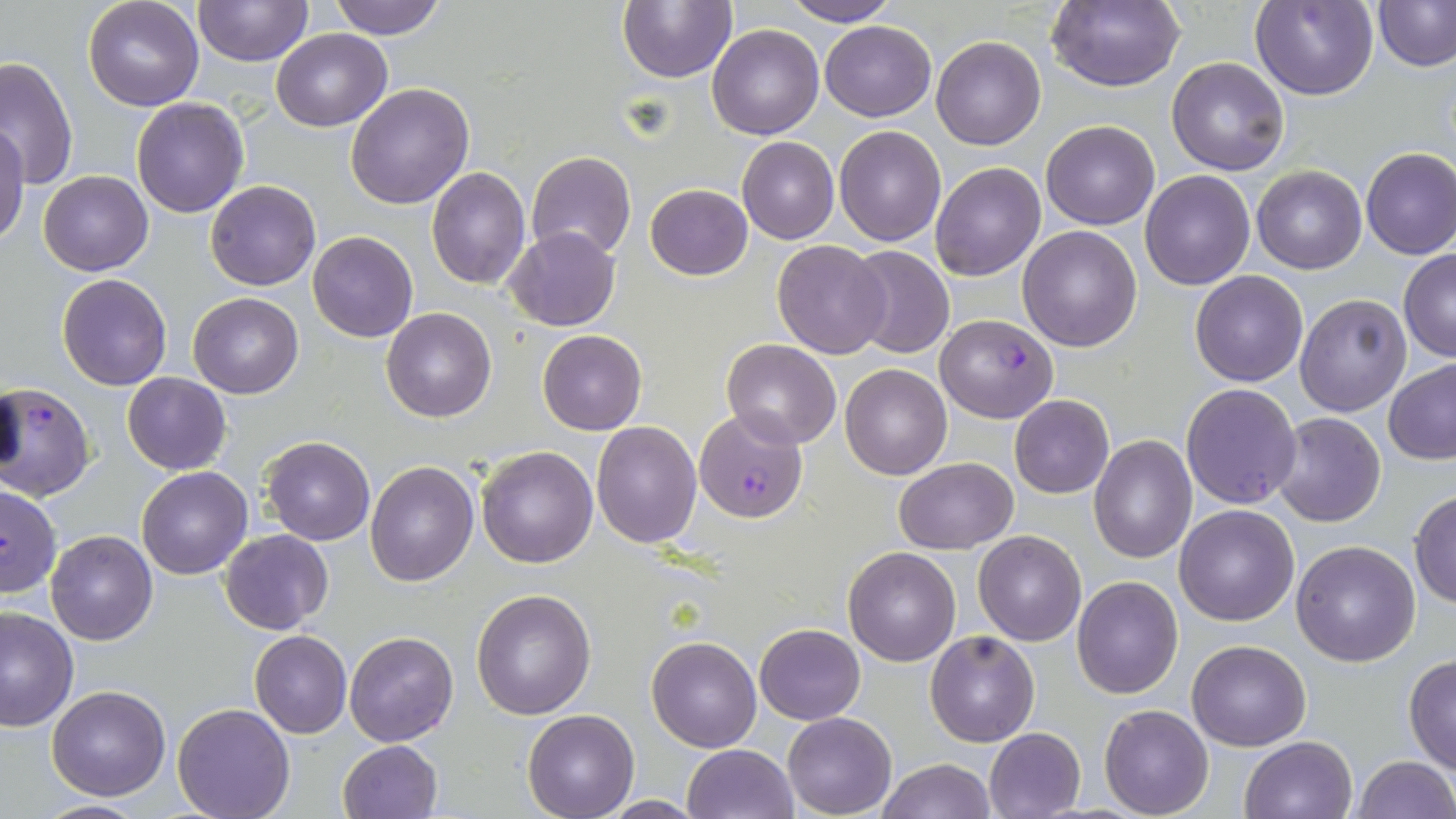
Approximate bounding boxes as named x1/y1/x2/y2 corners in pixels. Plasmodium falciparum-infected red blood cell locations: (x1=935, y1=313, x2=1059, y2=422), (x1=1, y1=382, x2=96, y2=502), (x1=696, y1=407, x2=808, y2=521), (x1=1, y1=483, x2=63, y2=598). Uninfected red blood cell locations: (x1=193, y1=0, x2=311, y2=66), (x1=328, y1=0, x2=448, y2=40), (x1=618, y1=0, x2=737, y2=83), (x1=782, y1=0, x2=900, y2=26), (x1=1253, y1=0, x2=1379, y2=101), (x1=1374, y1=0, x2=1456, y2=71), (x1=82, y1=1, x2=204, y2=111), (x1=1046, y1=1, x2=1186, y2=92), (x1=820, y1=21, x2=936, y2=121), (x1=707, y1=23, x2=824, y2=139), (x1=273, y1=28, x2=391, y2=130), (x1=931, y1=36, x2=1045, y2=151), (x1=0, y1=55, x2=77, y2=191), (x1=1167, y1=56, x2=1289, y2=175), (x1=345, y1=83, x2=474, y2=210), (x1=131, y1=98, x2=249, y2=219), (x1=0, y1=119, x2=30, y2=244), (x1=1041, y1=120, x2=1160, y2=230), (x1=834, y1=127, x2=945, y2=246), (x1=738, y1=137, x2=839, y2=244), (x1=1360, y1=146, x2=1456, y2=260), (x1=526, y1=150, x2=637, y2=261), (x1=930, y1=162, x2=1046, y2=282), (x1=426, y1=167, x2=530, y2=289), (x1=1252, y1=167, x2=1366, y2=274), (x1=1139, y1=169, x2=1256, y2=291), (x1=39, y1=170, x2=153, y2=276), (x1=205, y1=179, x2=321, y2=291), (x1=645, y1=183, x2=752, y2=280), (x1=1017, y1=226, x2=1143, y2=350), (x1=505, y1=227, x2=621, y2=332), (x1=308, y1=230, x2=418, y2=342), (x1=772, y1=239, x2=892, y2=358), (x1=845, y1=245, x2=956, y2=359), (x1=1398, y1=250, x2=1456, y2=360), (x1=1190, y1=270, x2=1307, y2=387), (x1=57, y1=273, x2=172, y2=390), (x1=188, y1=291, x2=303, y2=399), (x1=1294, y1=293, x2=1413, y2=416), (x1=382, y1=308, x2=497, y2=422), (x1=536, y1=329, x2=647, y2=434), (x1=722, y1=338, x2=841, y2=448), (x1=1383, y1=360, x2=1455, y2=464), (x1=841, y1=364, x2=952, y2=480), (x1=121, y1=372, x2=232, y2=475), (x1=1180, y1=383, x2=1302, y2=509), (x1=1009, y1=395, x2=1113, y2=499), (x1=1271, y1=412, x2=1386, y2=527), (x1=591, y1=421, x2=703, y2=549), (x1=261, y1=434, x2=376, y2=545), (x1=1088, y1=436, x2=1197, y2=563), (x1=476, y1=446, x2=599, y2=566), (x1=895, y1=458, x2=1018, y2=553), (x1=366, y1=460, x2=479, y2=586), (x1=137, y1=466, x2=252, y2=580), (x1=1409, y1=489, x2=1456, y2=608), (x1=1173, y1=504, x2=1299, y2=625), (x1=45, y1=529, x2=158, y2=646), (x1=219, y1=529, x2=334, y2=636), (x1=973, y1=530, x2=1086, y2=646), (x1=1290, y1=541, x2=1421, y2=666), (x1=844, y1=546, x2=961, y2=665), (x1=1072, y1=575, x2=1182, y2=699), (x1=472, y1=589, x2=598, y2=720), (x1=0, y1=605, x2=77, y2=731), (x1=754, y1=623, x2=865, y2=724), (x1=925, y1=629, x2=1040, y2=746), (x1=249, y1=630, x2=351, y2=738), (x1=345, y1=630, x2=458, y2=746), (x1=647, y1=637, x2=761, y2=752), (x1=1187, y1=638, x2=1310, y2=750), (x1=1403, y1=655, x2=1456, y2=774), (x1=46, y1=684, x2=172, y2=800), (x1=172, y1=703, x2=294, y2=819), (x1=1100, y1=704, x2=1214, y2=817), (x1=522, y1=710, x2=637, y2=819), (x1=783, y1=713, x2=895, y2=817), (x1=983, y1=727, x2=1087, y2=818), (x1=1240, y1=735, x2=1357, y2=819), (x1=337, y1=739, x2=442, y2=819), (x1=682, y1=744, x2=798, y2=819), (x1=1352, y1=755, x2=1455, y2=819), (x1=876, y1=759, x2=996, y2=818), (x1=599, y1=795, x2=705, y2=817), (x1=31, y1=799, x2=153, y2=817). Slide-level diagnosis: Plasmodium falciparum. Image is 1456×819 pixels. One field of a larger specimen. 1000x magnification. May-Grünwald-Giemsa stain. Optical microscopy. Thin blood film.